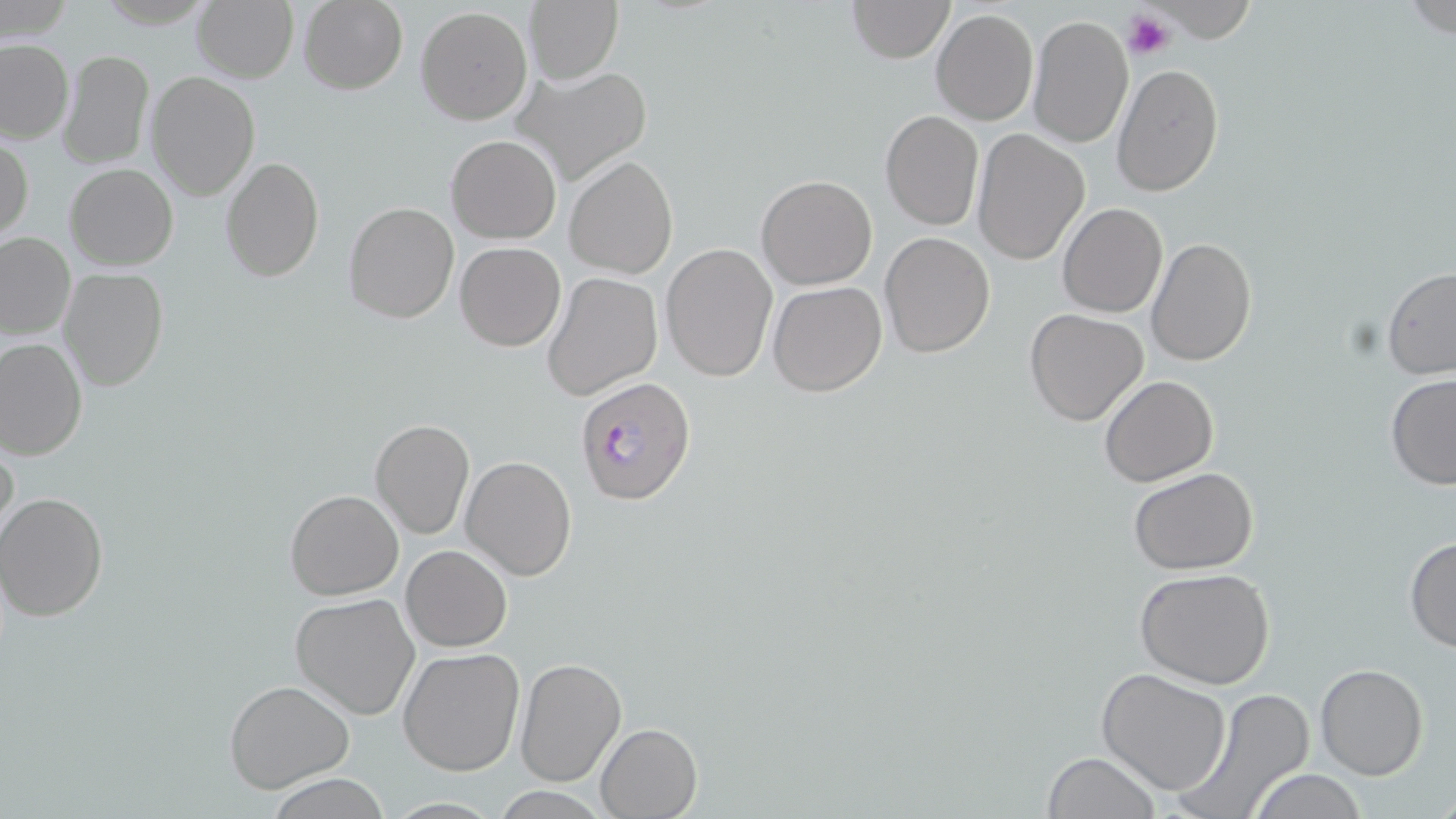

slide_level_diagnosis: Plasmodium falciparum
stain: May-Grünwald-Giemsa
plasmodium_falciparum_infected_red_blood_cell_locations: 'approximate bounding boxes as (x1,y1)-(x2,y2) corner pairs in pixels: (575,376)-(698,506)'
field_of_view: single
uninfected_red_blood_cell_locations: 'approximate bounding boxes as (x1,y1)-(x2,y2) corner pairs in pixels: (298,0)-(409,94), (525,0)-(624,86), (845,1)-(955,63), (192,2)-(297,82), (416,6)-(533,124), (931,8)-(1038,125), (1028,14)-(1134,152), (1,37)-(76,144), (58,49)-(155,171), (1110,63)-(1225,197), (511,64)-(653,187), (147,73)-(260,200), (878,110)-(984,231), (971,129)-(1089,264), (1,132)-(33,244), (446,134)-(561,242), (565,154)-(679,279), (221,155)-(325,283), (65,163)-(177,270), (755,173)-(878,290), (343,201)-(460,323), (1057,204)-(1168,318), (0,231)-(75,340), (879,232)-(996,358), (1144,236)-(1258,367), (454,242)-(565,351), (660,243)-(778,380), (58,266)-(169,391), (1381,266)-(1456,380), (541,271)-(663,401), (769,281)-(888,398), (1023,308)-(1149,427), (0,337)-(87,461), (1385,375)-(1456,490), (1099,376)-(1218,486), (370,419)-(475,540), (0,434)-(20,551), (460,455)-(577,580), (1128,468)-(1259,575), (284,489)-(403,600), (0,491)-(108,621), (1404,537)-(1456,654), (401,545)-(512,652), (1134,566)-(1279,689), (290,593)-(422,721), (398,646)-(525,776), (514,658)-(628,787), (1315,663)-(1428,780), (1096,667)-(1235,796), (224,677)-(355,794), (1170,687)-(1318,819), (595,722)-(703,818), (1041,752)-(1163,819), (1246,768)-(1369,819), (263,775)-(395,817)'
preparation: thin blood film
modality: light microscopy
magnification: 1000x
image_size: 1456×819 pixels
platelet_locations: 'approximate bounding boxes as (x1,y1)-(x2,y2) corner pairs in pixels: (1123,9)-(1176,61)'